Assess this cell for malaria.
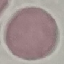
It is uninfected.

Photographed with a smartphone camera at the microscope eyepiece. Thin smear of blood. Giemsa-stained preparation. Automatically extracted cell patch, resized to 64 × 64 pixels.